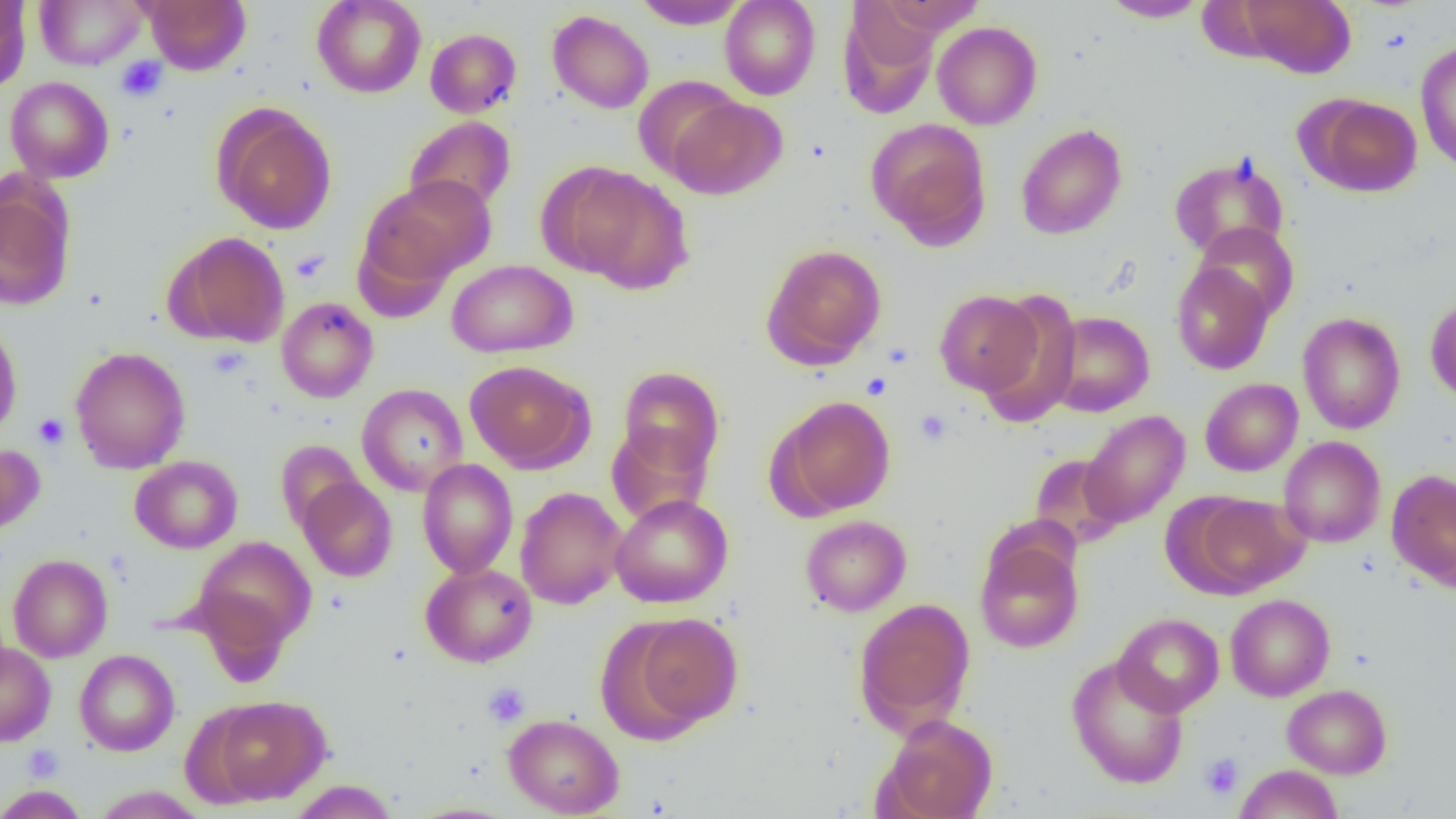
Approximate bounding boxes as (x1, y1, x2, y2) in pixels. Platelet locations: (117, 56, 167, 102), (290, 249, 329, 284), (863, 372, 892, 400), (916, 410, 952, 444), (34, 414, 69, 449), (482, 682, 530, 727), (22, 744, 64, 782), (1200, 752, 1244, 800). Uninfected red blood cell locations: (0, 0, 31, 94), (35, 0, 145, 69), (143, 0, 251, 75), (312, 0, 426, 98), (634, 0, 748, 29), (719, 0, 820, 100), (874, 0, 988, 35), (1239, 0, 1355, 78), (1099, 1, 1208, 22), (839, 3, 940, 117), (547, 10, 654, 114), (932, 21, 1042, 130), (424, 27, 522, 118), (1415, 40, 1456, 173), (632, 75, 742, 181), (5, 76, 114, 182), (1307, 94, 1422, 196), (666, 96, 788, 200), (213, 104, 337, 235), (404, 116, 516, 214), (866, 117, 991, 247), (1015, 123, 1128, 240), (1169, 154, 1289, 261), (556, 165, 694, 292), (361, 175, 496, 289), (0, 183, 75, 311), (1192, 222, 1299, 324), (169, 231, 290, 348), (761, 243, 887, 368), (446, 259, 578, 357), (1171, 260, 1274, 375), (976, 288, 1081, 427), (934, 290, 1042, 396), (1425, 296, 1456, 404), (276, 297, 378, 403), (1046, 311, 1155, 417), (1297, 312, 1406, 434), (0, 320, 22, 440), (69, 346, 190, 474), (464, 360, 594, 473), (616, 366, 724, 478), (361, 375, 594, 488), (1200, 378, 1303, 476), (356, 383, 469, 496), (773, 396, 896, 517), (1079, 410, 1190, 528), (605, 422, 715, 525), (1279, 436, 1386, 548), (275, 440, 366, 534), (0, 444, 45, 538), (1029, 453, 1128, 549), (130, 455, 243, 554), (417, 459, 518, 578), (1387, 469, 1456, 589), (297, 471, 516, 576), (298, 477, 397, 582), (515, 486, 627, 609), (610, 493, 733, 608), (1185, 494, 1308, 596), (799, 514, 911, 616), (975, 535, 1084, 654), (193, 537, 317, 652), (8, 554, 113, 662), (420, 562, 538, 667), (1225, 594, 1335, 701), (853, 598, 976, 734), (1113, 612, 1224, 717), (626, 613, 743, 733), (0, 641, 56, 746), (74, 649, 180, 755), (1067, 655, 1189, 790), (1282, 684, 1392, 778), (207, 695, 328, 805), (503, 713, 624, 818), (880, 713, 998, 819), (1234, 764, 1343, 819), (288, 780, 399, 819), (1, 785, 89, 818), (91, 785, 208, 818). Slide-level diagnosis: negative for blood parasites. Light microscopy. Single field of view. 1000x magnification. Thin blood film. Image is 1456×819 pixels.